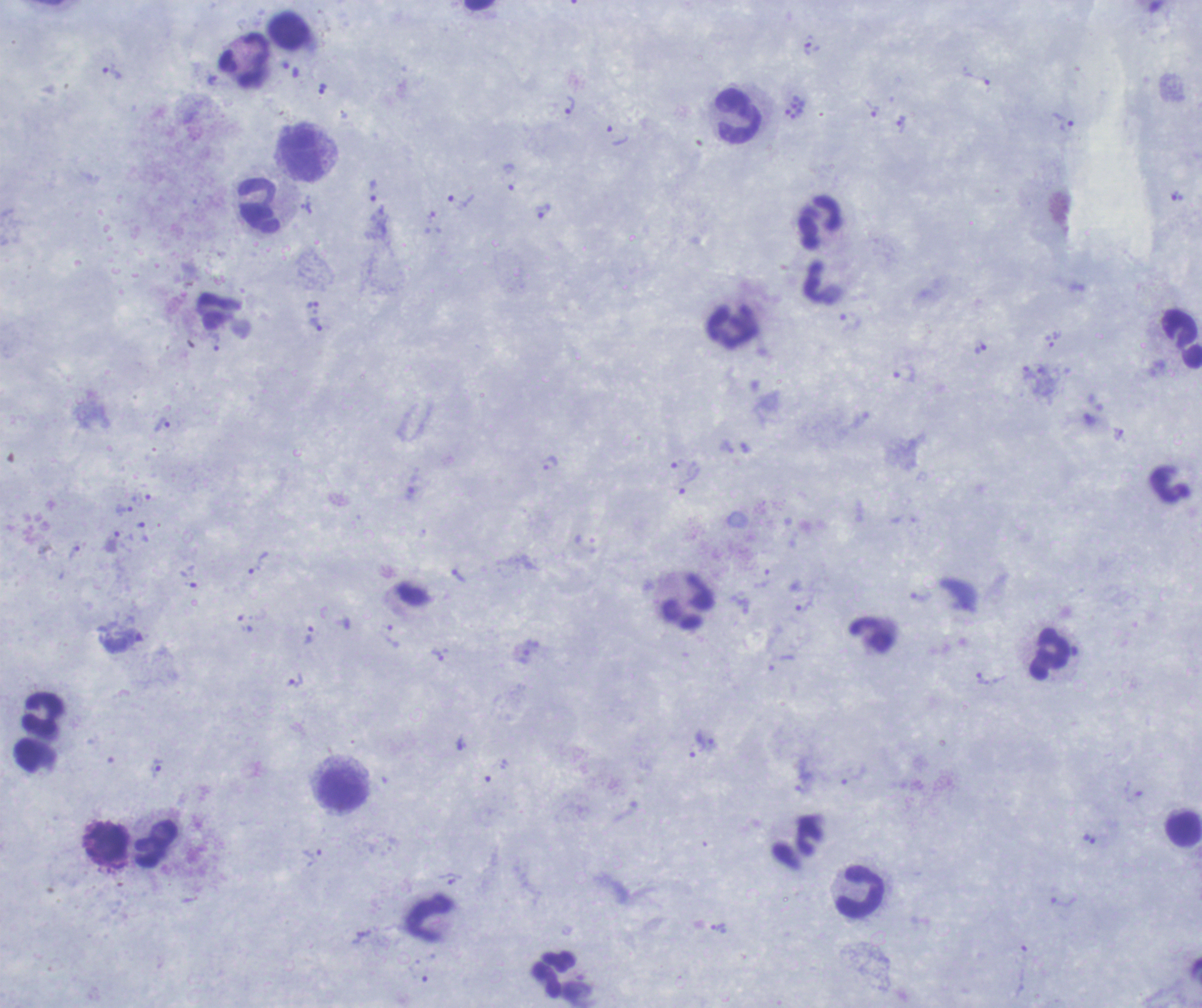 Thick smear of blood. Romanowsky-stained preparation. One field from this slide. Image is 1202×1008 pixels.